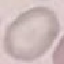

result = negative for malaria parasites
preparation = thin blood smear
image type = automatically extracted cell patch, resized to 64 × 64 pixels
stain = Giemsa
capture = smartphone through the microscope eyepiece